Assess the morphology of the red blood cells.
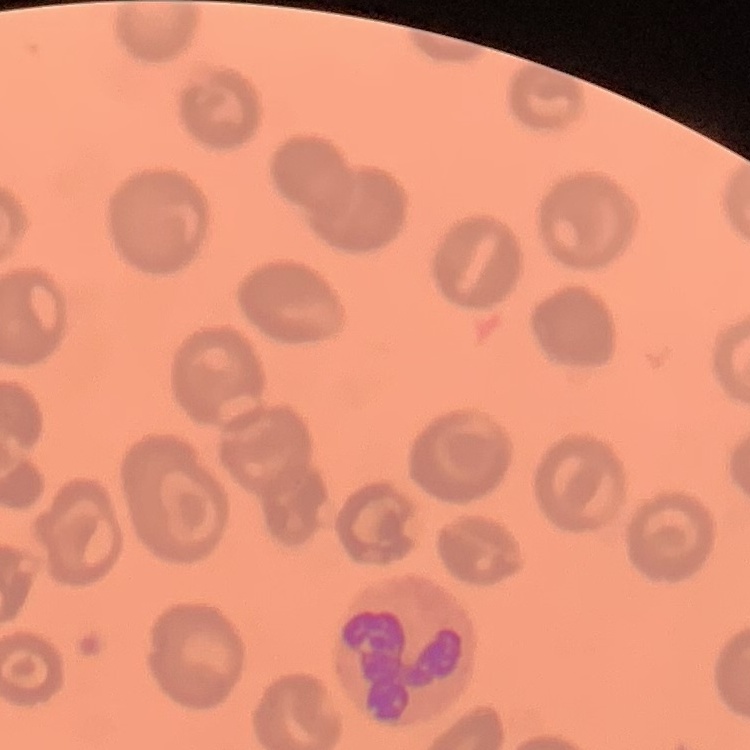

They show no rouleaux formation.

Thin peripheral smear. Field's or Giemsa stain. One tile cut from a larger photomicrograph.